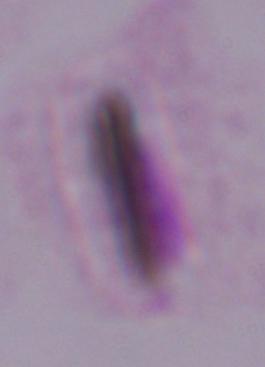
Summary:
  - Magnification: 1000x
  - Identification: trichomonad
  - Modality: photomicrograph